Outline Plasmodium parasites and white blood cells.
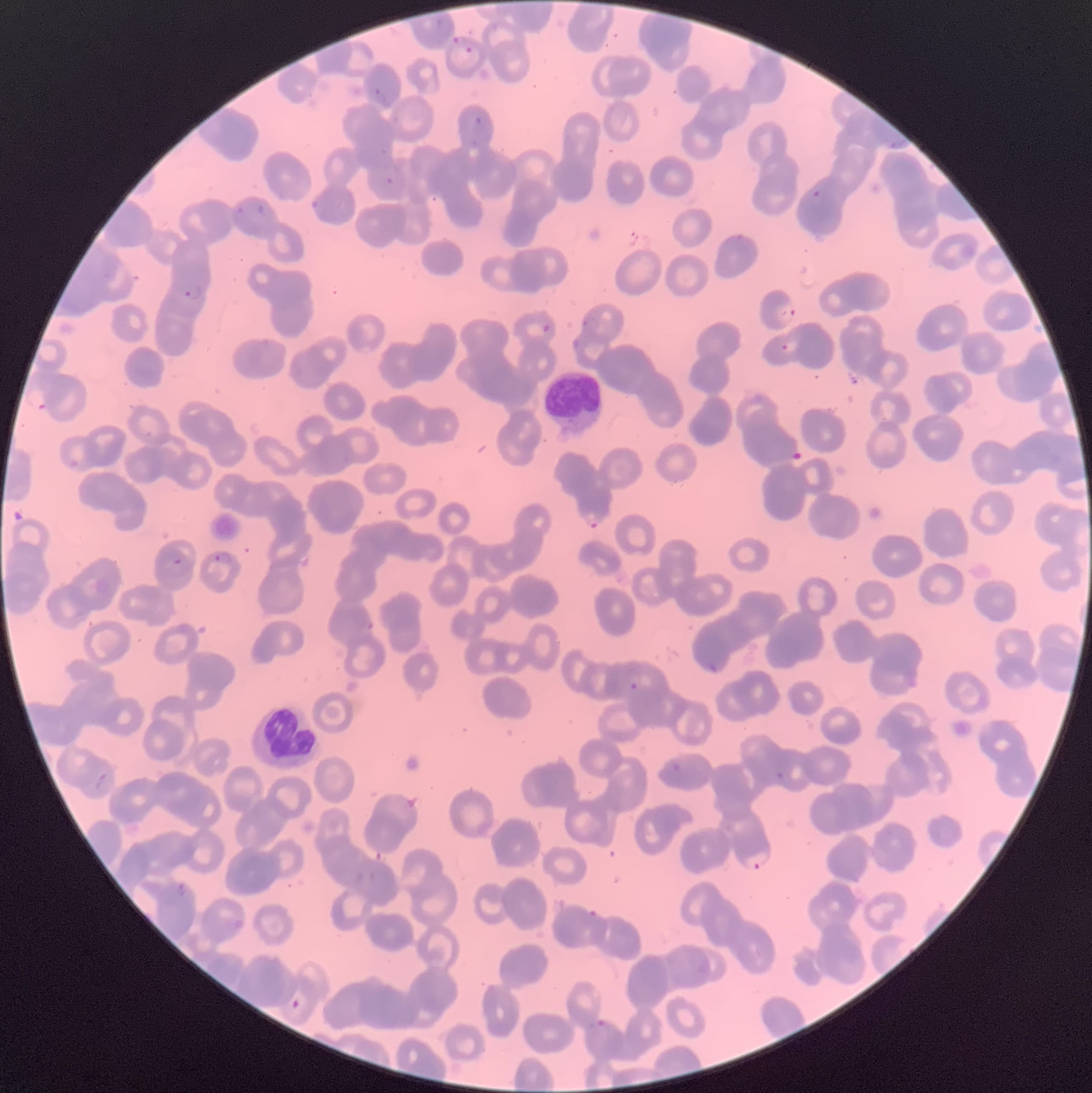

Approximate bounding boxes as (x1,y1)-(x2,y2) corner pairs in pixels.
Plasmodium parasites: (453,37)-(467,48), (465,46)-(474,53), (371,87)-(390,108), (471,117)-(486,134), (890,140)-(906,150), (385,177)-(394,186), (812,189)-(821,199), (311,196)-(322,212), (256,204)-(272,220), (235,206)-(248,218), (181,283)-(202,302), (778,301)-(797,325), (582,316)-(601,334), (542,323)-(551,334), (781,340)-(801,353), (584,512)-(604,531), (213,552)-(233,565), (173,557)-(183,565), (366,619)-(375,632), (704,660)-(720,674), (628,682)-(639,692), (670,762)-(682,773), (775,771)-(785,780), (744,850)-(773,870), (176,881)-(188,897), (291,999)-(300,1009), (595,1019)-(607,1028).
White blood cells: (545,370)-(602,437), (250,702)-(321,772).

Summary:
  - Image size: 1092×1093 pixels
  - Modality: optical microscopy
  - Preparation: thin blood film
  - Red blood cell morphology: rouleaux formation